Mark where platelets are.
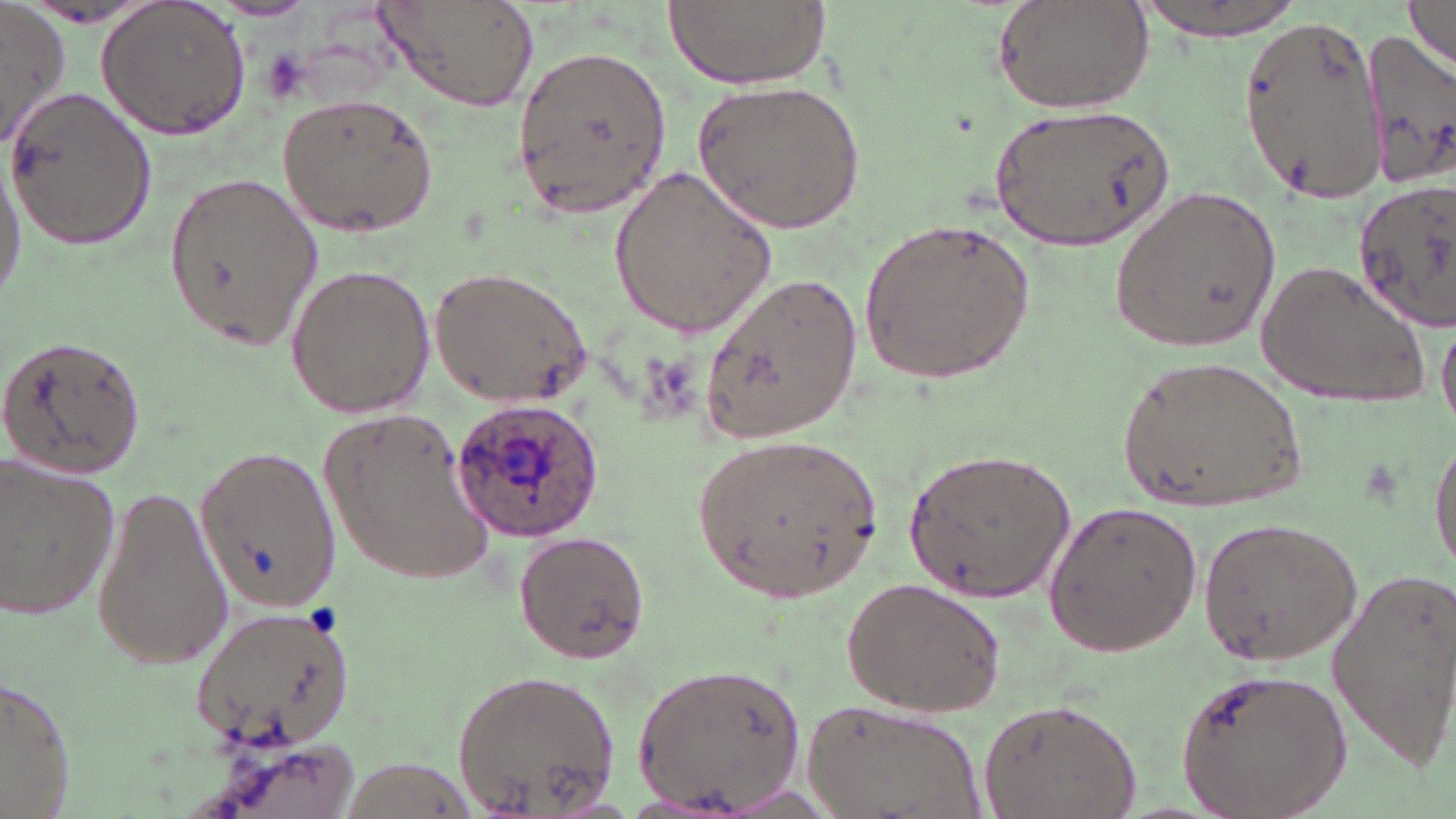
Approximate bounding boxes as (x1,y1)-(x2,y2) corner pairs in pixels.
Platelets: (258,48)-(309,105).

Uninfected red blood cell locations: (663,0)-(829,89), (992,0)-(1156,114), (1129,0)-(1309,40), (1403,1)-(1456,71), (210,2)-(318,21), (375,2)-(540,114), (1,3)-(71,149), (96,3)-(250,141), (1238,17)-(1388,204), (1357,30)-(1456,191), (512,43)-(671,224), (693,79)-(866,231), (4,83)-(158,253), (274,93)-(440,237), (988,102)-(1173,254), (0,153)-(26,310), (608,164)-(780,341), (161,168)-(325,353), (1352,179)-(1456,337), (1111,187)-(1280,353), (859,213)-(1034,390), (1254,261)-(1429,411), (282,264)-(437,420), (429,266)-(591,408), (700,270)-(860,447), (1437,312)-(1455,440), (0,336)-(144,482), (1119,355)-(1307,516), (322,408)-(496,583), (690,430)-(884,603), (1431,430)-(1456,578), (195,446)-(340,611), (904,447)-(1076,603), (0,457)-(122,623), (87,481)-(232,672), (1040,501)-(1204,659), (1196,516)-(1366,666), (512,531)-(651,664), (1323,564)-(1455,763), (840,577)-(1007,717), (188,602)-(355,752), (632,659)-(810,814), (1175,666)-(1349,819), (450,669)-(622,814), (0,677)-(77,815), (805,697)-(988,819), (976,698)-(1144,819). Plasmodium ovale-infected red blood cell locations: (448,397)-(606,543). Slide-level diagnosis: Plasmodium ovale. Thin blood smear. May-Grünwald-Giemsa-stained preparation. One field of a larger specimen. Image is 1456×819 pixels. Optical microscopy. Captured at 1000x magnification.